Comment on the morphology of the erythrocytes.
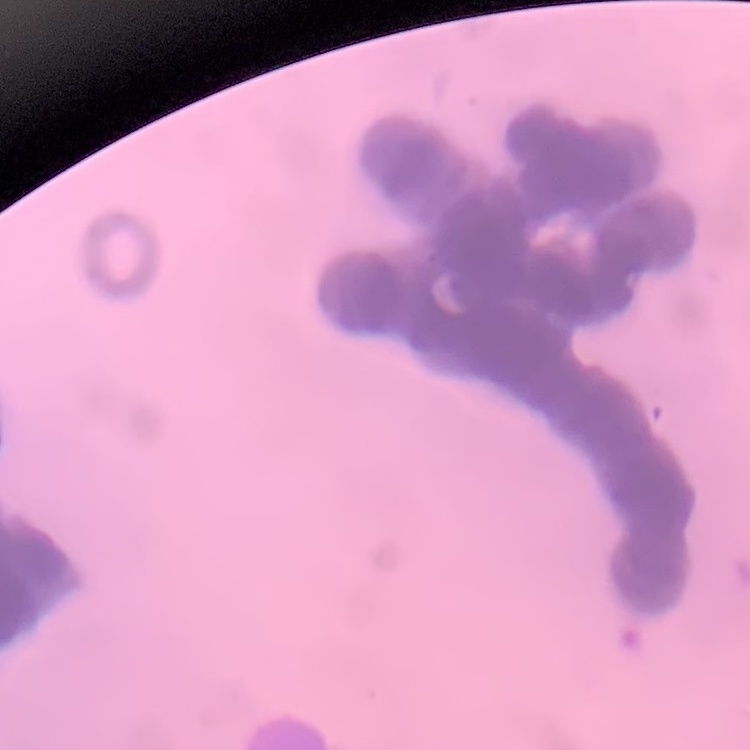

They show rouleaux formation.

Summary:
  - Preparation: thin blood film
  - Image type: one tile cut from a larger photomicrograph
  - Stain: Field's or Giemsa